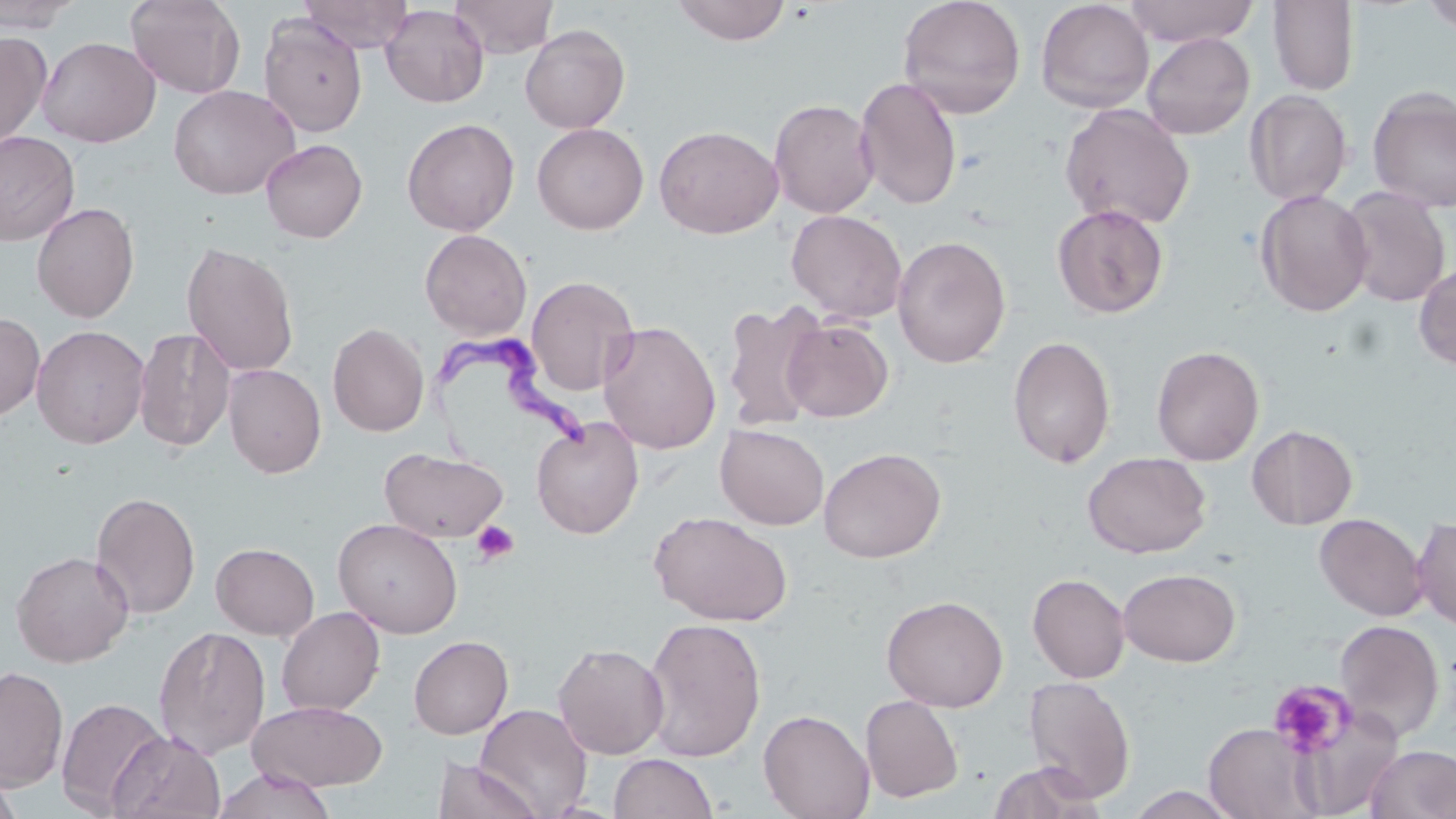
slide-level diagnosis = Trypanosoma brucei
preparation = thin blood film
stain = May-Grünwald-Giemsa
platelet locations = approximate bounding boxes as (x1, y1, x2, y2) in pixels: (471, 520, 519, 566), (1267, 680, 1354, 757)
uninfected red blood cell locations = approximate bounding boxes as (x1, y1, x2, y2) in pixels: (0, 0, 83, 33), (125, 0, 246, 98), (299, 0, 414, 52), (451, 0, 558, 58), (672, 0, 791, 45), (898, 0, 1026, 118), (1036, 0, 1155, 113), (1123, 0, 1260, 47), (1421, 0, 1456, 34), (1268, 1, 1360, 95), (381, 4, 489, 108), (259, 13, 368, 137), (520, 24, 630, 134), (0, 32, 51, 149), (1141, 32, 1255, 140), (37, 36, 160, 147), (855, 76, 962, 211), (167, 84, 300, 199), (1367, 87, 1456, 213), (1244, 89, 1352, 207), (769, 98, 879, 218), (1059, 103, 1195, 230), (402, 117, 520, 236), (532, 123, 649, 234), (654, 125, 783, 239), (0, 131, 80, 246), (261, 138, 367, 243), (1337, 187, 1451, 307), (1255, 189, 1374, 317), (31, 202, 140, 323), (1052, 204, 1169, 318), (786, 209, 908, 324), (419, 229, 532, 339), (892, 235, 1011, 368), (181, 239, 300, 378), (1414, 263, 1456, 370), (526, 274, 639, 396), (721, 300, 827, 433), (0, 312, 45, 423), (782, 319, 893, 422), (598, 320, 722, 454), (328, 322, 429, 437), (31, 325, 150, 449), (133, 327, 235, 452), (1007, 335, 1115, 469), (1151, 345, 1264, 466), (223, 364, 326, 479), (531, 417, 643, 539), (715, 423, 829, 530), (1247, 425, 1358, 530), (379, 446, 509, 543), (818, 447, 946, 563), (1083, 451, 1210, 558), (91, 492, 202, 619), (648, 510, 794, 627), (1314, 513, 1428, 621), (332, 517, 463, 638), (1412, 517, 1456, 630), (211, 542, 320, 640), (11, 550, 134, 667), (1118, 567, 1241, 666), (1027, 572, 1130, 683), (881, 594, 1008, 711), (276, 606, 385, 716), (641, 616, 767, 762), (1334, 619, 1444, 741), (154, 625, 271, 759), (408, 635, 513, 739), (553, 642, 669, 760), (0, 665, 68, 792), (1023, 675, 1136, 803), (860, 695, 964, 803), (56, 697, 169, 816), (248, 700, 388, 791), (475, 703, 593, 818), (758, 708, 875, 819), (1300, 713, 1394, 810), (1204, 723, 1319, 819), (108, 729, 226, 819), (1365, 745, 1456, 819), (609, 752, 718, 818), (431, 758, 543, 819), (986, 761, 1105, 818), (213, 767, 336, 819), (0, 772, 23, 819), (1124, 786, 1244, 818)
image size = 1456×819 pixels
magnification = 1000x
Trypanosoma brucei locations = approximate bounding boxes as (x1, y1, x2, y2) in pixels: (420, 324, 609, 490)
modality = optical microscopy
field of view = one of a larger specimen